Give the extent of all Plasmodium falciparum-infected red blood cells.
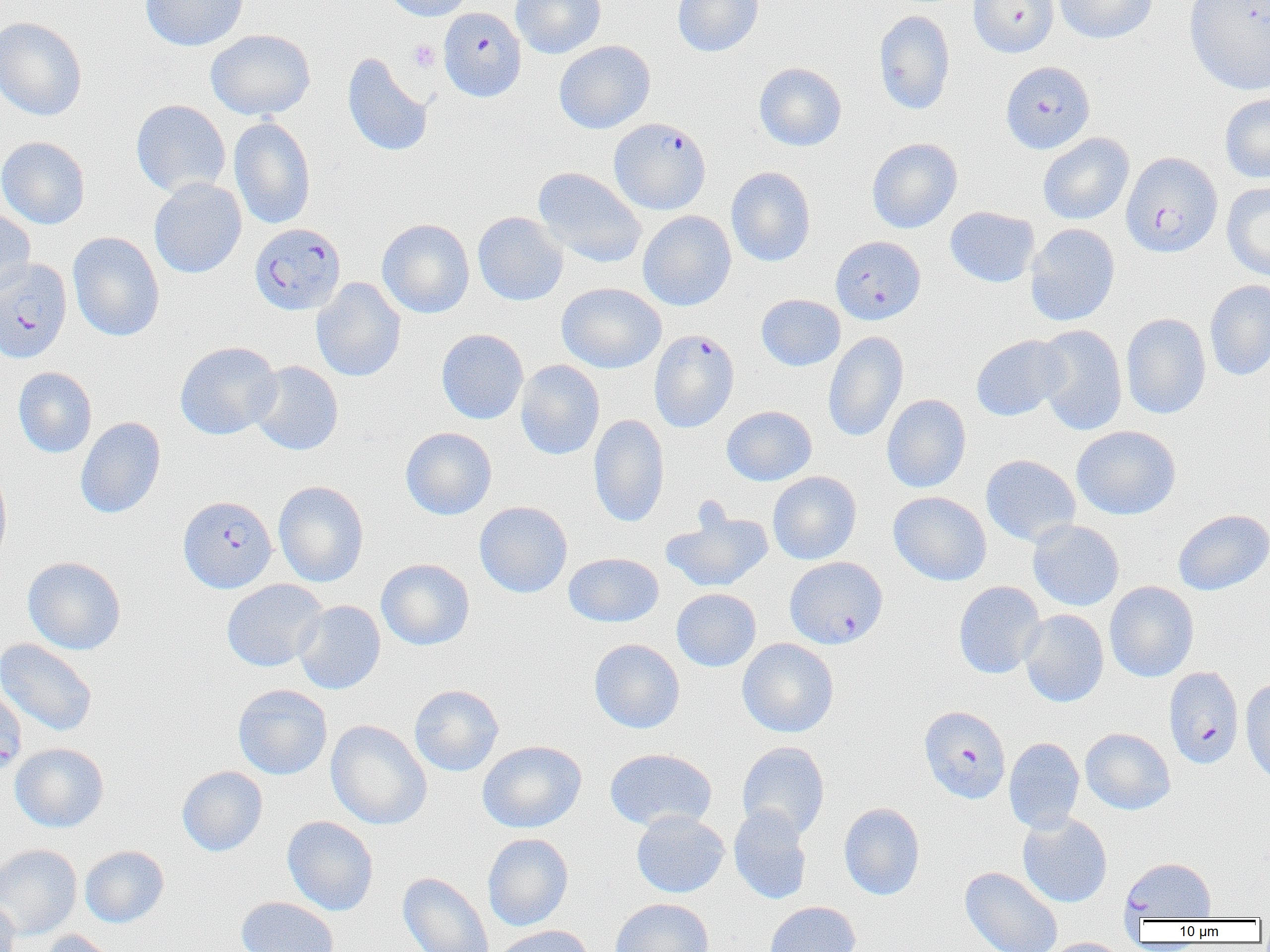

Approximate bounding boxes as (x1, y1, x2, y2) in pixels.
Plasmodium falciparum-infected red blood cells (subset): (968, 0, 1059, 58), (440, 10, 527, 104), (1000, 61, 1095, 154), (609, 117, 711, 214), (1121, 151, 1223, 257), (249, 223, 346, 315), (0, 258, 72, 363), (648, 329, 739, 433), (178, 495, 277, 593), (1163, 666, 1245, 769), (0, 686, 27, 780), (918, 706, 1011, 804), (1120, 857, 1216, 922).

Platelet locations: (407, 39, 440, 72). Uninfected red blood cell locations (subset): (140, 0, 249, 52), (382, 0, 475, 21), (510, 0, 606, 58), (672, 0, 763, 57), (1054, 0, 1158, 44), (1184, 0, 1270, 96), (873, 10, 955, 114), (0, 17, 88, 121), (205, 29, 316, 120), (554, 40, 655, 134), (342, 53, 433, 157), (754, 62, 847, 151), (1220, 93, 1270, 183), (131, 99, 231, 198), (229, 116, 316, 230), (1037, 133, 1134, 225), (1, 136, 90, 229), (867, 137, 963, 233), (533, 167, 646, 268), (726, 167, 816, 267), (149, 178, 247, 278), (1221, 182, 1270, 282), (945, 206, 1040, 288), (0, 207, 36, 299), (638, 210, 736, 311), (473, 211, 568, 306), (377, 218, 475, 318), (1025, 223, 1120, 327), (67, 231, 165, 341), (311, 277, 406, 381), (1204, 280, 1270, 380), (557, 282, 667, 373), (756, 294, 845, 371), (1121, 313, 1211, 419), (1035, 324, 1128, 436), (436, 328, 528, 425), (823, 331, 909, 443), (971, 335, 1068, 421), (175, 341, 282, 440), (515, 360, 605, 460), (249, 361, 343, 456), (13, 367, 97, 458), (881, 394, 971, 493), (722, 405, 817, 485), (588, 414, 670, 528), (75, 416, 166, 519), (1072, 425, 1182, 520), (400, 427, 497, 520), (980, 454, 1081, 547), (0, 463, 12, 568), (768, 471, 861, 564), (273, 480, 369, 587), (888, 491, 991, 586), (474, 501, 572, 598), (662, 505, 774, 593), (1172, 509, 1270, 596), (1027, 520, 1124, 611), (564, 553, 664, 626), (23, 556, 126, 655), (376, 558, 474, 651), (221, 579, 327, 671), (953, 581, 1046, 679), (1104, 581, 1199, 682), (671, 588, 761, 671), (294, 600, 386, 694), (1019, 609, 1109, 707), (0, 638, 98, 736), (589, 638, 685, 733), (737, 638, 839, 737), (1240, 676, 1270, 786), (232, 684, 333, 780), (409, 684, 504, 776), (326, 720, 432, 830), (1080, 727, 1175, 815), (1004, 737, 1085, 834), (477, 740, 587, 833), (737, 741, 830, 840), (10, 743, 109, 832), (604, 748, 717, 832), (177, 766, 268, 856), (838, 802, 925, 900), (729, 805, 812, 905), (631, 810, 730, 898), (1017, 813, 1112, 908), (282, 816, 379, 915), (483, 833, 574, 931), (0, 844, 82, 940), (80, 845, 169, 928), (960, 866, 1063, 952), (398, 872, 494, 952), (236, 896, 339, 952), (0, 897, 20, 952), (611, 898, 713, 952), (764, 900, 861, 952), (491, 925, 595, 952), (37, 930, 125, 952), (1041, 937, 1128, 952). Slide-level diagnosis: Plasmodium falciparum. Single field of view. Light microscopy. Captured at 1000x magnification. Thin blood film. Image is 1270×952 pixels.